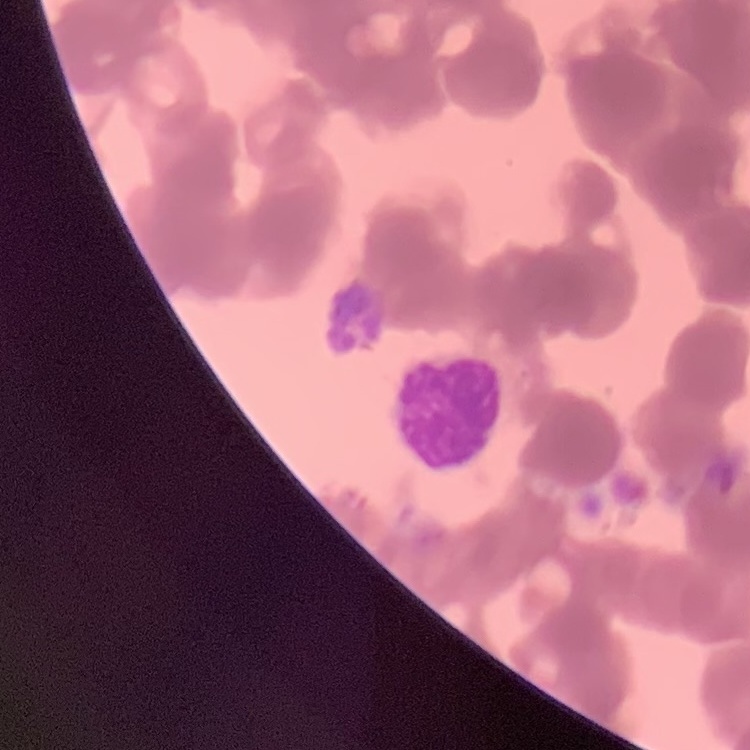
The red blood cells exhibit rouleaux formation. One tile cut from a larger photomicrograph. Field's or Giemsa stain. Thin peripheral smear.